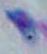
Summary:
  - Modality: micrograph
  - Identification: Toxoplasma gondii
  - Magnification: 1000x